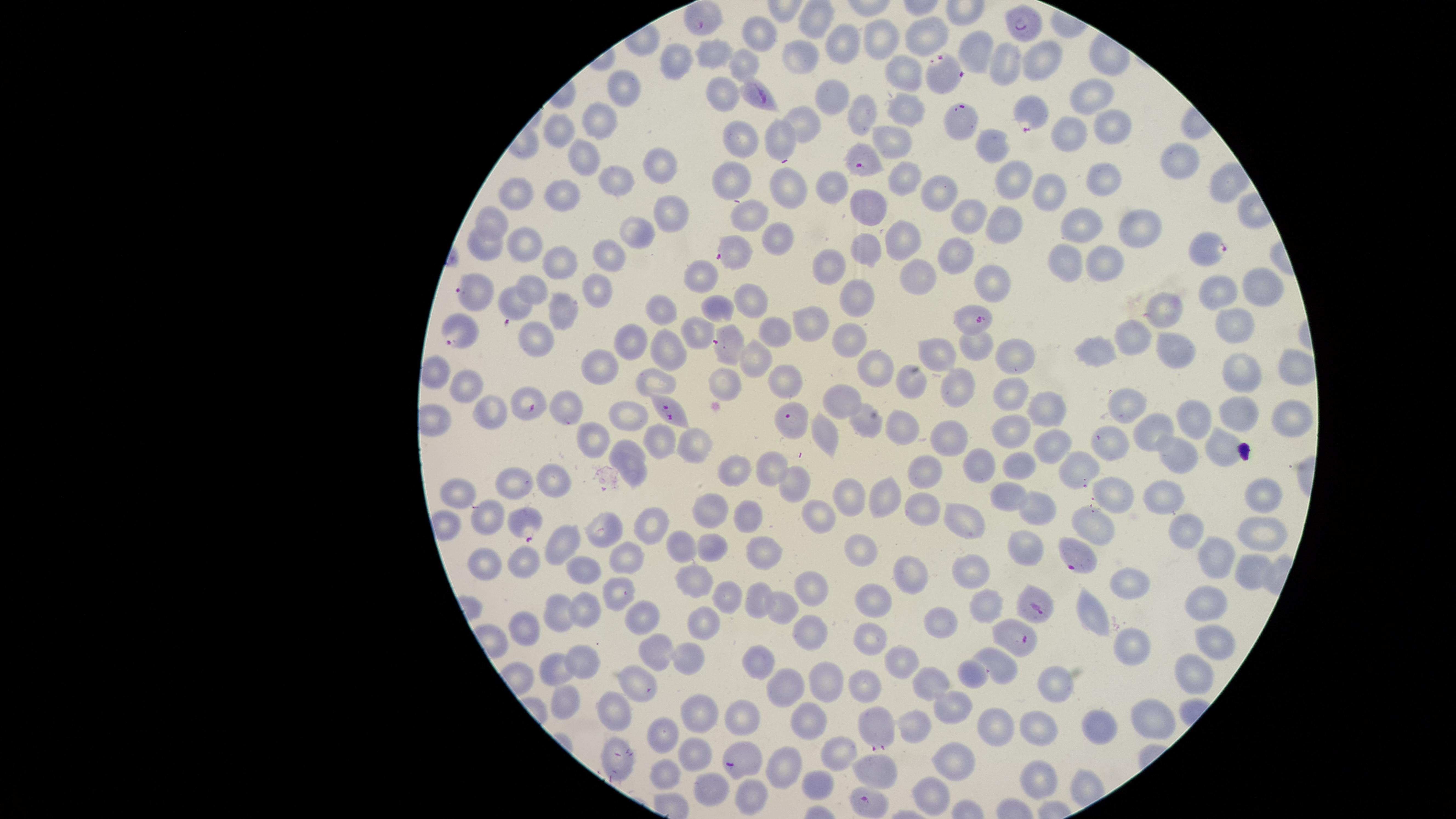
Approximate marker points as (x, y) in pixels. Uninfected RBCs: (813, 19), (927, 34), (759, 35), (884, 39), (843, 44), (975, 47), (715, 52), (800, 54), (1044, 58), (1010, 60), (675, 62), (746, 63), (901, 74), (623, 88), (719, 93), (1090, 95), (833, 103), (907, 107), (862, 111), (597, 123), (800, 127), (1113, 127), (562, 131), (1068, 134), (891, 136), (734, 140), (778, 140), (993, 143), (585, 154), (1170, 161), (655, 163), (902, 176), (617, 178), (1014, 178), (1102, 179), (733, 184), (1225, 184), (830, 188), (935, 190), (793, 191), (1045, 191), (520, 192), (563, 197), (870, 197), (669, 212), (967, 212), (752, 216), (496, 217), (1007, 222), (1082, 222), (1144, 229), (634, 232), (776, 239), (898, 239), (482, 245), (526, 245), (863, 250), (953, 252), (608, 256), (1104, 257), (1068, 263), (555, 264), (827, 264), (997, 273), (696, 277), (923, 279), (1252, 285), (535, 286), (597, 289), (1211, 294), (852, 298), (748, 299), (511, 304), (1167, 305), (565, 309), (711, 309), (661, 316), (809, 321), (1227, 325), (694, 332), (774, 333), (1133, 336), (853, 340), (631, 341), (975, 343), (1168, 348), (1098, 352), (937, 353), (669, 355), (1019, 356), (752, 359), (875, 363), (599, 365), (1238, 367), (1288, 368), (784, 375), (908, 380), (471, 383), (959, 387), (1012, 398), (838, 407), (490, 410), (569, 410), (1044, 410), (1126, 410), (1237, 412), (627, 416), (1284, 416), (1197, 417), (595, 427), (903, 429), (1147, 429), (824, 431), (1013, 431), (949, 439), (1109, 439), (1053, 443), (624, 444), (660, 445), (1218, 446), (696, 447), (1178, 455), (972, 460), (770, 463), (1016, 463), (734, 465), (1079, 468), (638, 470), (923, 473), (561, 478), (517, 480), (795, 481), (1267, 490), (1009, 492), (1116, 492), (1164, 493), (458, 495), (850, 495), (883, 498), (1041, 506), (709, 510), (922, 510), (489, 514), (752, 515), (817, 515), (966, 517), (654, 523), (1096, 523), (1187, 528), (1260, 531), (603, 532), (1020, 543), (568, 546), (683, 546), (865, 548), (1219, 549), (715, 552), (761, 553), (623, 559), (486, 561), (529, 563), (1251, 565), (976, 572), (584, 575), (906, 576), (1128, 579), (688, 581), (812, 589), (619, 593), (755, 595), (726, 599), (881, 600), (983, 601), (1202, 601), (783, 608), (560, 610), (587, 611), (1092, 613), (942, 617), (641, 618), (700, 624), (526, 629), (808, 633), (869, 637), (1217, 642), (1137, 643), (657, 651), (685, 655), (897, 660), (580, 661), (762, 661), (1001, 665), (550, 670), (1187, 672), (971, 673), (635, 683), (860, 683), (930, 683), (822, 684), (1053, 686), (789, 687), (565, 701), (613, 704), (954, 706), (701, 713), (739, 718), (1153, 718), (806, 721), (919, 721), (993, 722), (1038, 723), (1103, 724), (668, 736), (838, 751), (694, 756), (622, 759), (954, 759), (785, 765), (878, 773), (666, 775), (1041, 777), (711, 779), (820, 784), (925, 795), (742, 802). Parasitized RBCs: (700, 17), (1024, 25), (941, 67), (755, 95), (1030, 108), (957, 111), (863, 161), (1210, 244), (736, 248), (475, 294), (973, 318), (458, 333), (728, 343), (529, 405), (670, 412), (791, 419), (525, 522), (1078, 555), (1035, 609), (1017, 637), (875, 728), (740, 758), (873, 799). Presence: malaria parasites identified. Giemsa stain. One field of view of the specimen. The visible region is circular. Image is 1456×819 pixels. Photographed with a smartphone camera through the microscope eyepiece. Thin blood film. Species: Plasmodium falciparum.